State the preparation type.
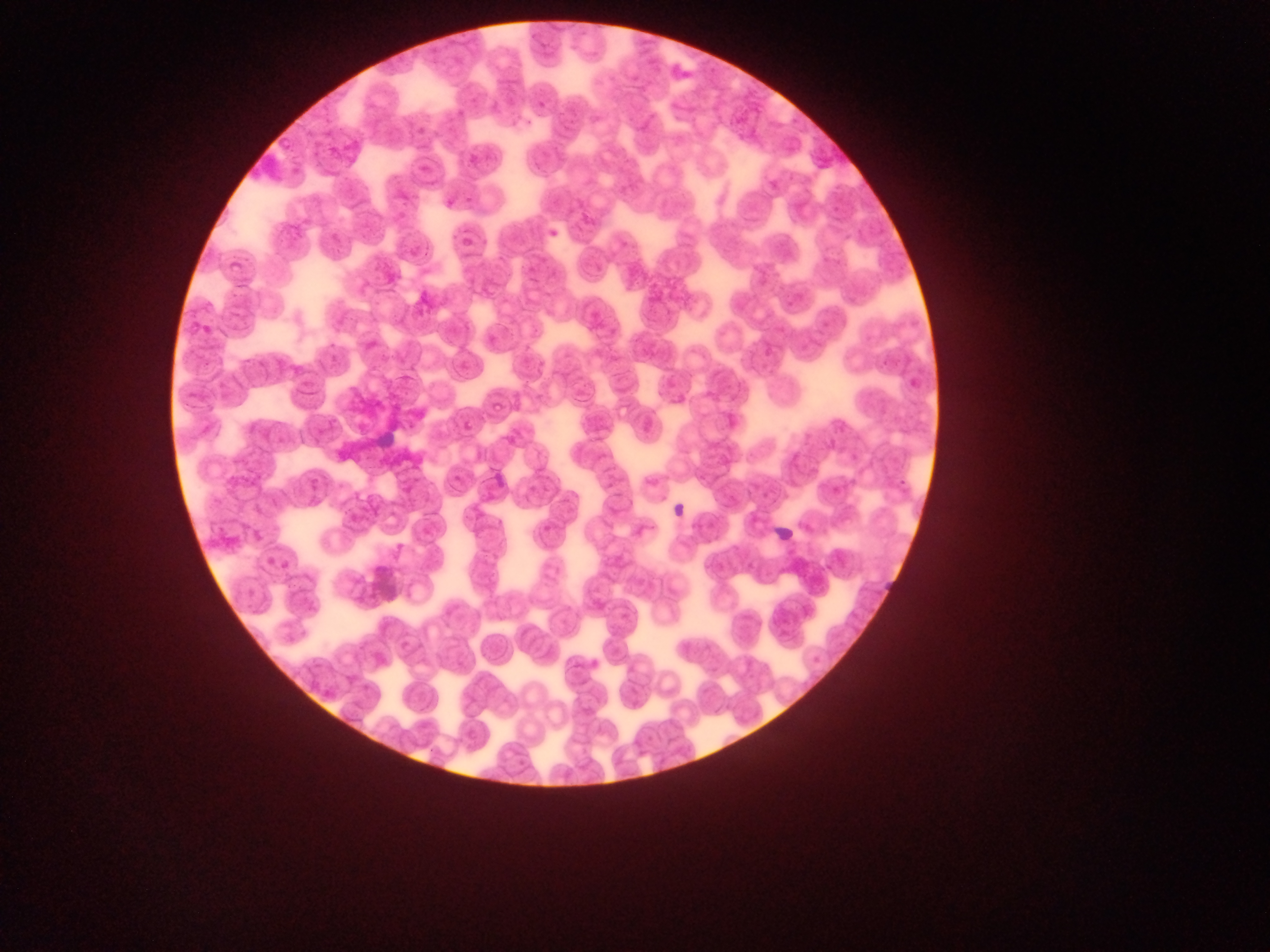
This is a thin smear.

image size = 1270×952 pixels
capture = mobile-phone photograph through a microscope
Plasmodium parasite locations = approximate bounding boxes as (left, top, right, bottom) in pixels: (539, 99, 548, 111), (525, 117, 534, 129), (415, 124, 427, 135), (470, 154, 483, 170), (765, 178, 784, 196), (466, 194, 474, 207), (830, 200, 839, 214), (545, 230, 562, 238), (458, 236, 478, 246), (785, 299, 796, 310), (822, 317, 831, 337), (201, 323, 216, 337), (798, 341, 808, 353), (766, 345, 779, 359), (878, 358, 890, 370), (459, 360, 476, 377), (911, 376, 921, 386), (493, 402, 508, 413), (462, 419, 482, 433), (826, 434, 838, 453), (850, 447, 866, 468), (452, 471, 464, 483), (834, 477, 846, 498), (899, 477, 913, 488), (750, 481, 763, 493), (542, 522, 555, 535), (418, 525, 434, 537), (249, 527, 258, 537), (265, 554, 276, 569), (275, 557, 292, 571), (245, 585, 259, 600), (810, 652, 823, 671), (591, 657, 600, 668), (466, 728, 482, 742)
country = Ghana
leukocyte locations = approximate bounding boxes as (left, top, right, bottom) in pixels: (247, 142, 293, 193), (376, 429, 401, 449), (671, 498, 701, 529), (767, 522, 794, 546)
field of view = single